Comment on the morphology of the red blood cells.
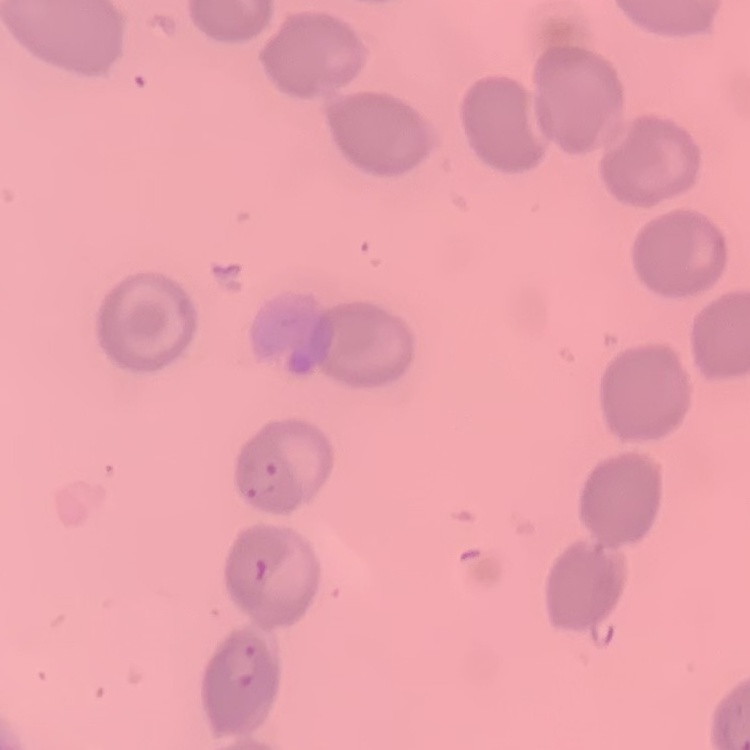
They show no rouleaux formation.

Square crop of a larger photomicrograph. Field's or Giemsa stain. Thin blood smear.